State which parasite is depicted.
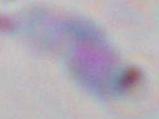

This is Toxoplasma gondii.

Micrograph. 1000x magnification.